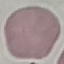
Result: no malaria parasites seen. Acquired by smartphone through the microscope eyepiece. Cell patch, automatically extracted from a larger field of view and resized to 64 × 64 pixels. Giemsa-stained preparation. Thin smear of blood.